Classify this cell by malaria status.
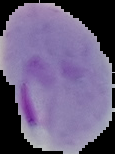
It is parasitized.

Summary:
  - Image size: 115×154 pixels
  - Preparation: thin blood smear
  - Image type: segmented cell region with the area outside set to black